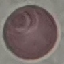
malaria_status: uninfected
preparation: thin smear
stain: Giemsa
capture: smartphone through the microscope eyepiece
image_type: automatically extracted cell patch, resized to 64 × 64 pixels